Report the malaria status of this cell.
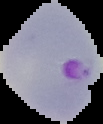

It is parasitized.

From a thin blood smear. Cell region segmented out of the field of view; the surrounding area is masked to black. Image is 103×124 pixels.